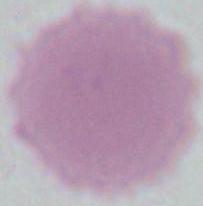

{
  "modality": "micrograph",
  "magnification": "1000x",
  "identification": "erythrocyte"
}